Give the preparation type.
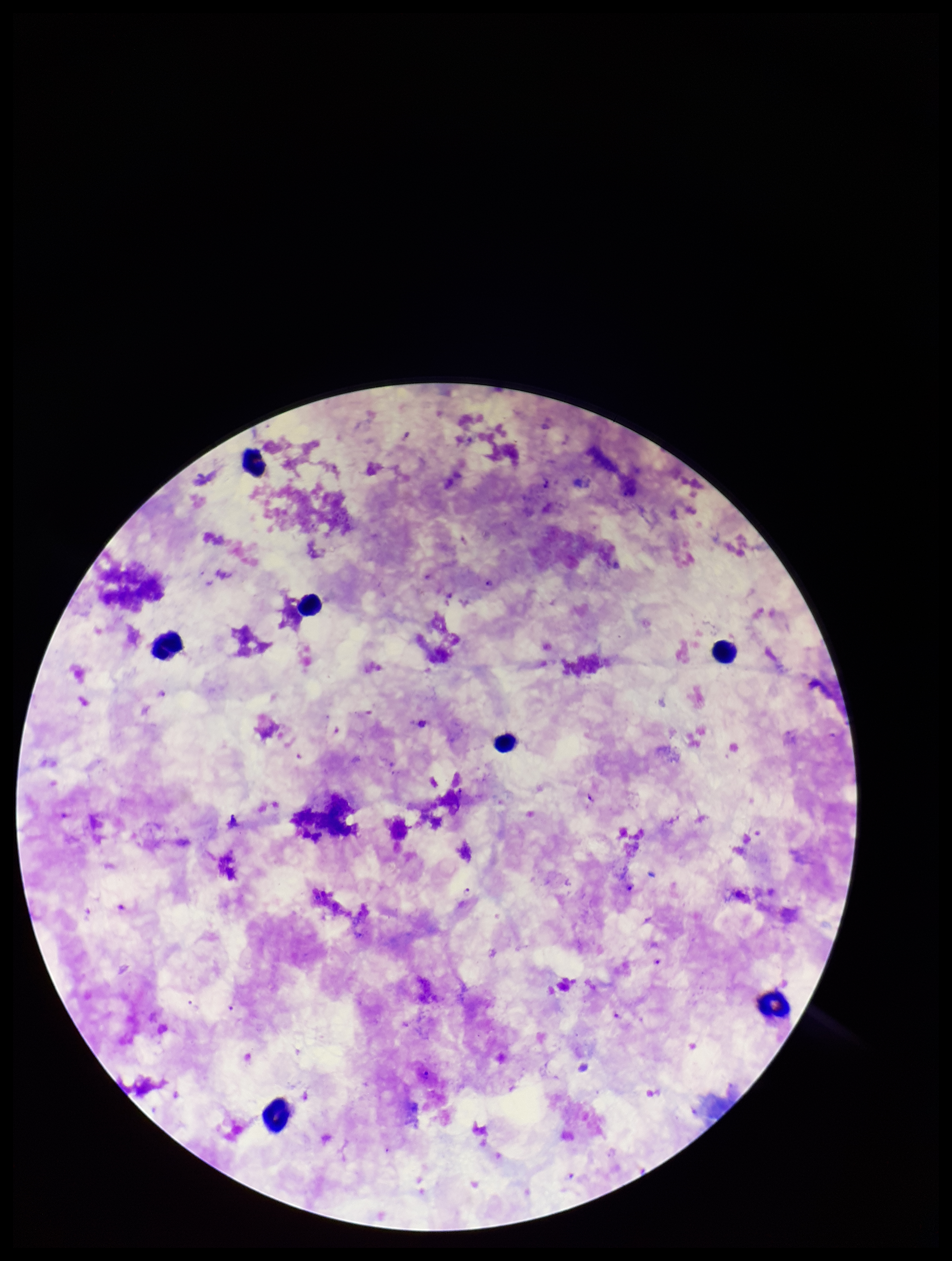
A thick smear.

Leukocyte count: 7. Plasmodium parasites: seen. Parasite count: 5. Patient malaria status: positive. Species reported for this patient: Plasmodium falciparum. Single field of view. Image is 952×1261 pixels. Stained with Giemsa. Photographed through the microscope eyepiece with a smartphone camera.